Name the cell type shown.
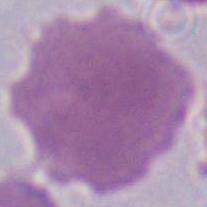
This is an erythrocyte.

magnification: 1000x
modality: micrograph